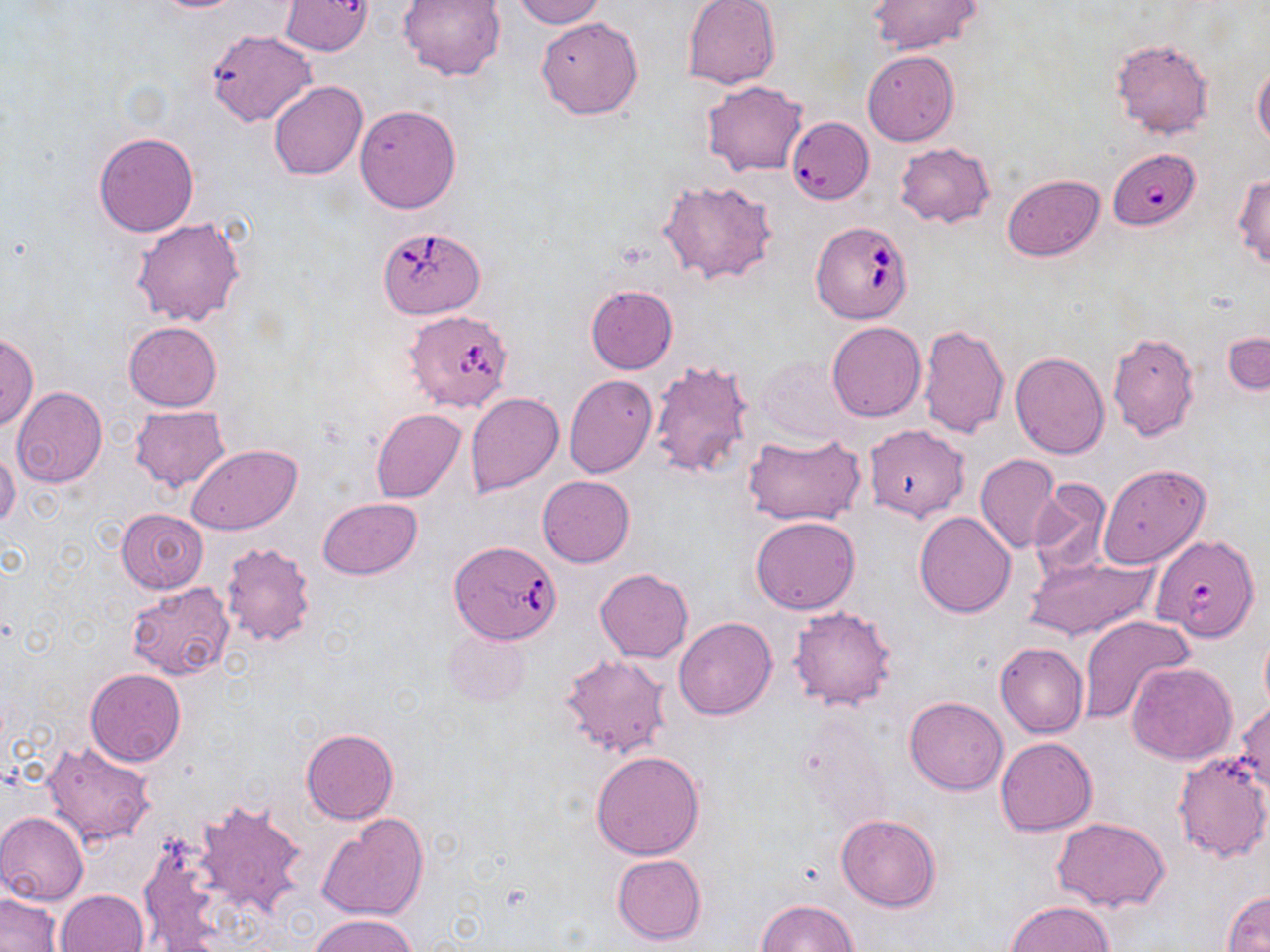

Summary:
  - Coordinate format: approximate bounding boxes as (x1,y1)-(x2,y2) corner pairs in pixels
  - Uninfected red blood cell locations: (147,0)-(250,12), (398,0)-(507,80), (512,0)-(605,28), (280,1)-(373,56), (682,1)-(781,89), (867,1)-(983,54), (536,16)-(643,120), (205,29)-(317,125), (1110,39)-(1214,141), (863,50)-(960,146), (1253,65)-(1270,147), (269,81)-(368,179), (703,81)-(809,176), (355,103)-(461,213), (785,116)-(873,206), (93,132)-(200,237), (895,142)-(995,227), (1231,172)-(1270,270), (1003,173)-(1105,260), (658,177)-(780,286), (131,217)-(243,327), (585,286)-(677,374), (123,321)-(222,411), (827,322)-(926,422), (917,324)-(1009,437), (1224,330)-(1270,396), (1108,332)-(1200,440), (0,333)-(39,432), (1010,352)-(1109,459), (757,357)-(851,442), (649,359)-(756,480), (563,375)-(657,477), (11,387)-(107,488), (464,392)-(564,497), (129,406)-(230,493), (372,408)-(465,503), (862,424)-(970,521), (741,431)-(866,528), (188,444)-(301,534), (0,448)-(21,531), (975,454)-(1061,553), (1097,463)-(1211,568), (537,475)-(634,567), (1029,480)-(1113,578), (318,498)-(421,578), (116,507)-(209,595), (914,511)-(1015,617), (752,516)-(859,614), (219,542)-(316,647), (1023,555)-(1158,640), (594,568)-(693,662), (126,584)-(233,679), (788,605)-(898,711), (1080,615)-(1194,724), (674,618)-(777,721), (443,627)-(532,707), (995,641)-(1089,738), (560,653)-(672,759), (1125,662)-(1238,764), (85,668)-(186,766), (905,696)-(1007,795), (1232,698)-(1270,794), (301,727)-(399,824), (994,737)-(1097,837), (41,738)-(158,849), (591,749)-(705,859), (1171,751)-(1270,865), (194,799)-(307,917), (0,811)-(89,905), (317,813)-(429,923), (836,814)-(942,911), (1053,817)-(1173,912), (137,838)-(225,947), (611,853)-(708,946), (57,889)-(148,952), (1222,889)-(1270,951), (0,893)-(61,952), (756,899)-(858,952), (1006,901)-(1113,952), (307,913)-(418,952)
  - Babesia divergens-infected red blood cell locations: (1109,149)-(1200,230), (810,221)-(913,324), (378,224)-(486,319), (402,309)-(514,413), (1150,533)-(1260,640), (450,539)-(562,645)
  - Slide-level diagnosis: Babesia divergens
  - Field of view: single
  - Modality: optical microscopy
  - Magnification: 1000x
  - Stain: May-Grünwald-Giemsa
  - Image size: 1270×952 pixels
  - Preparation: thin blood smear